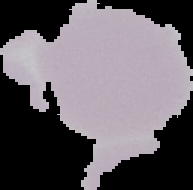
From a thin blood smear. Result: no malaria parasites seen. Image is 193×190 pixels. Cell region segmented out of the field of view; the surrounding area is masked to black.